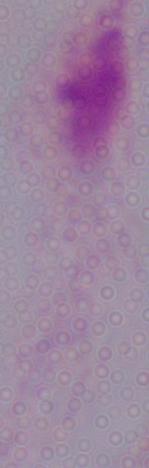 A trichomonad is seen. 1000x magnification. Photomicrograph.